Report the malaria status of this cell.
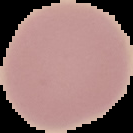

Uninfected.

Summary:
  - Image type: cell region segmented out of the field of view; surrounding area masked to black
  - Image size: 133×133 pixels
  - Preparation: thin blood film